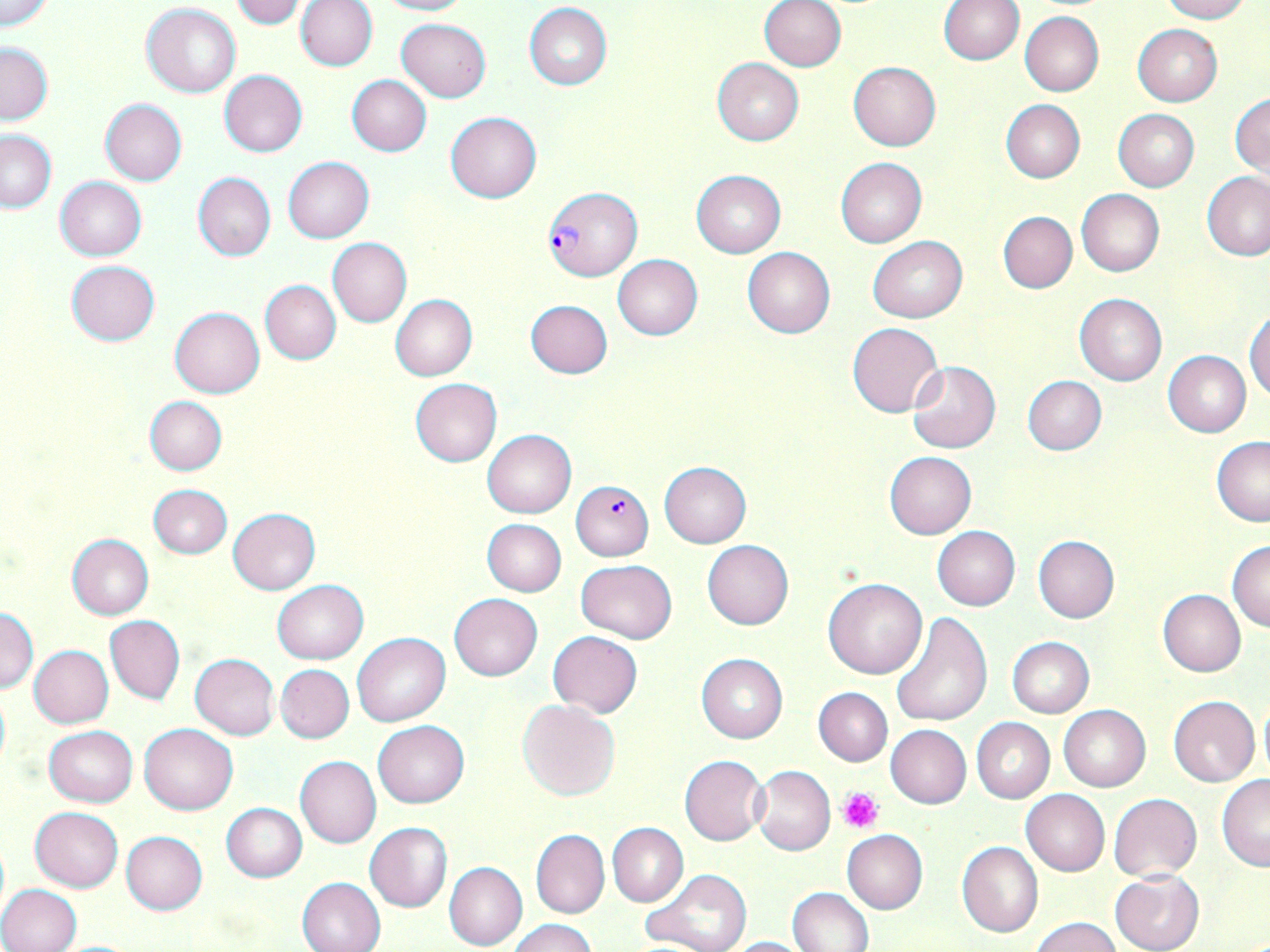

slide-level diagnosis = Plasmodium falciparum
image size = 1270×952 pixels
field of view = single
preparation = thin blood smear
uninfected red blood cell locations = approximate bounding boxes as [x1, y1, x2, y2] in pixels: [0, 0, 52, 29], [229, 0, 309, 29], [372, 0, 472, 16], [939, 0, 1023, 65], [1160, 0, 1251, 22], [296, 1, 378, 71], [759, 1, 846, 72], [525, 3, 612, 89], [141, 4, 240, 97], [1020, 12, 1103, 96], [395, 19, 491, 102], [1132, 24, 1222, 107], [0, 42, 53, 126], [711, 58, 804, 146], [848, 61, 941, 151], [218, 70, 308, 156], [346, 75, 433, 155], [1230, 92, 1269, 178], [99, 98, 187, 186], [1001, 99, 1085, 182], [1112, 109, 1199, 191], [445, 111, 542, 203], [1, 129, 56, 212], [283, 156, 373, 243], [835, 158, 927, 248], [692, 169, 785, 257], [1201, 171, 1270, 261], [192, 173, 275, 261], [55, 176, 147, 260], [1076, 189, 1164, 276], [997, 211, 1077, 293], [867, 236, 967, 322], [328, 239, 412, 327], [741, 247, 836, 338], [612, 254, 702, 340], [66, 261, 160, 345], [259, 280, 341, 364], [1075, 293, 1166, 385], [390, 295, 477, 380], [525, 300, 613, 378], [170, 307, 265, 398], [1246, 308, 1270, 402], [847, 323, 943, 416], [1164, 351, 1250, 436], [907, 361, 1001, 454], [1022, 375, 1107, 454], [410, 379, 502, 467], [144, 396, 227, 475], [481, 429, 576, 518], [1211, 437, 1270, 526], [884, 452, 977, 538], [658, 461, 752, 547], [149, 485, 231, 558], [228, 508, 320, 595], [482, 518, 567, 597], [931, 526, 1021, 610], [66, 533, 154, 620], [1033, 536, 1120, 624], [703, 539, 794, 630], [1228, 541, 1270, 631], [576, 560, 676, 642], [823, 579, 927, 679], [271, 581, 368, 664], [1158, 589, 1246, 676], [450, 594, 542, 681], [0, 607, 39, 695], [892, 612, 992, 729], [106, 616, 185, 705], [548, 630, 642, 717], [352, 633, 450, 726], [1007, 637, 1094, 718], [30, 645, 114, 728], [189, 654, 279, 739], [696, 654, 787, 742], [275, 664, 354, 743], [0, 687, 10, 774], [813, 687, 892, 765], [1168, 695, 1259, 787], [1258, 695, 1270, 784], [517, 700, 619, 801], [1059, 705, 1151, 790], [971, 717, 1055, 803], [372, 720, 470, 808], [139, 723, 238, 814], [886, 724, 971, 808], [44, 726, 137, 807], [679, 755, 768, 844], [295, 756, 381, 848], [752, 766, 835, 855], [1216, 775, 1270, 871], [1021, 789, 1110, 876], [1108, 793, 1202, 882], [222, 803, 307, 882], [29, 808, 123, 893], [364, 822, 453, 912], [608, 823, 688, 907], [531, 829, 609, 918], [842, 829, 928, 914], [120, 831, 207, 915], [957, 841, 1043, 937], [444, 862, 527, 951], [640, 868, 752, 952], [1109, 870, 1205, 952], [297, 877, 386, 952], [0, 884, 82, 952], [787, 887, 874, 952], [1030, 916, 1121, 952], [507, 918, 596, 952], [724, 935, 814, 952], [48, 939, 145, 952]
Plasmodium falciparum-infected red blood cell locations = approximate bounding boxes as [x1, y1, x2, y2] in pixels: [544, 189, 641, 284], [571, 480, 654, 560]
stain = May-Grünwald-Giemsa
platelet locations = approximate bounding boxes as [x1, y1, x2, y2] in pixels: [838, 786, 884, 832]
magnification = 1000x
modality = light microscopy